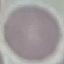
malaria status = uninfected
capture = smartphone through the microscope eyepiece
stain = Giemsa
preparation = thin blood film
image type = cell patch, automatically extracted from a larger field of view and resized to 64 × 64 pixels